Find the red blood cells that are infected with P. falciparum, and any of indeterminate infection status.
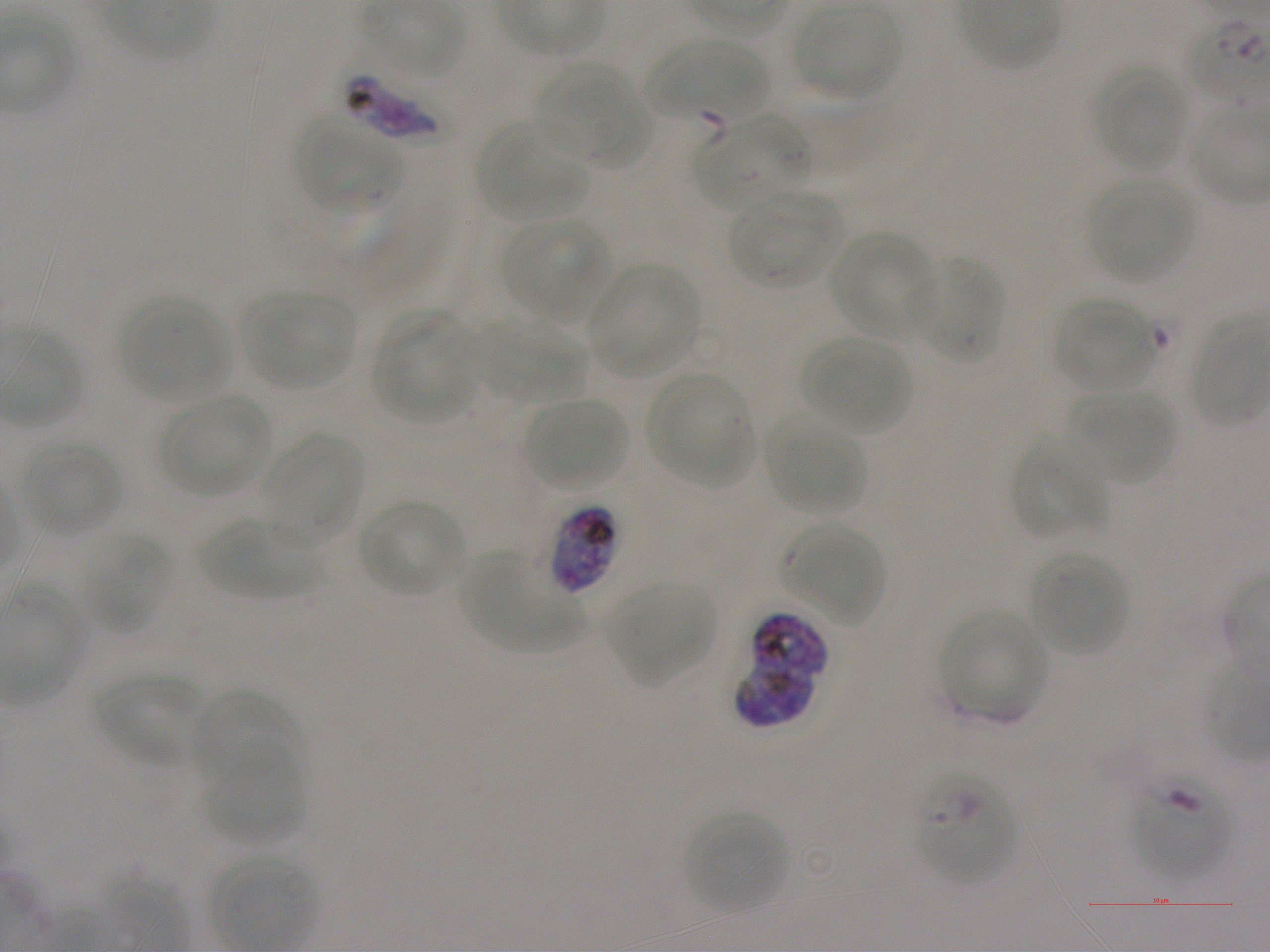

Approximate bounding boxes as {x1, y1, x2, y2} in pixels. Not every red blood cell is marked. A life-cycle stage — or a range of stages, where the recorded stages span more than one — follows each staged infected red blood cell.
Infected red blood cells: {345, 71, 448, 144}; {548, 503, 619, 595} late trophozoite to late schizont; {736, 612, 826, 726}; {912, 771, 1017, 884} ring.
Red blood cells of indeterminate infection status: {1130, 780, 1232, 882}.

Locations of uninfected red blood cells: {795, 5, 904, 101}, {646, 38, 768, 118}, {536, 64, 644, 165}, {1094, 67, 1188, 172}, {691, 112, 810, 214}, {296, 115, 399, 216}, {475, 124, 587, 221}, {1088, 177, 1194, 283}, {728, 189, 845, 291}, {501, 219, 610, 321}, {831, 233, 937, 339}, {907, 255, 1008, 363}, {588, 263, 699, 375}, {243, 291, 358, 391}, {120, 297, 232, 400}, {1053, 298, 1157, 393}, {372, 312, 475, 422}, {466, 317, 590, 405}, {801, 337, 910, 437}, {645, 372, 756, 488}, {1070, 389, 1176, 486}, {161, 397, 269, 497}, {524, 397, 629, 491}, {764, 416, 867, 516}, {258, 433, 363, 540}, {1012, 436, 1104, 537}, {24, 441, 124, 537}, {360, 499, 465, 598}, {198, 516, 320, 600}, {785, 522, 886, 627}, {82, 536, 173, 633}, {1029, 552, 1128, 655}, {462, 554, 581, 653}, {606, 582, 717, 683}, {939, 609, 1047, 721}, {97, 674, 203, 766}, {189, 689, 301, 785}, {204, 749, 308, 848}, {685, 812, 787, 912}, {213, 853, 314, 943}. Thin blood film. Blood group of the donor: A+. Static in-vitro culture of P. falciparum strain NF54. Giemsa-stained preparation. Image is 1270×952 pixels. Single field of view. Oil immersion, 100x objective (numerical aperture 1.25).